Name the blood parasite species.
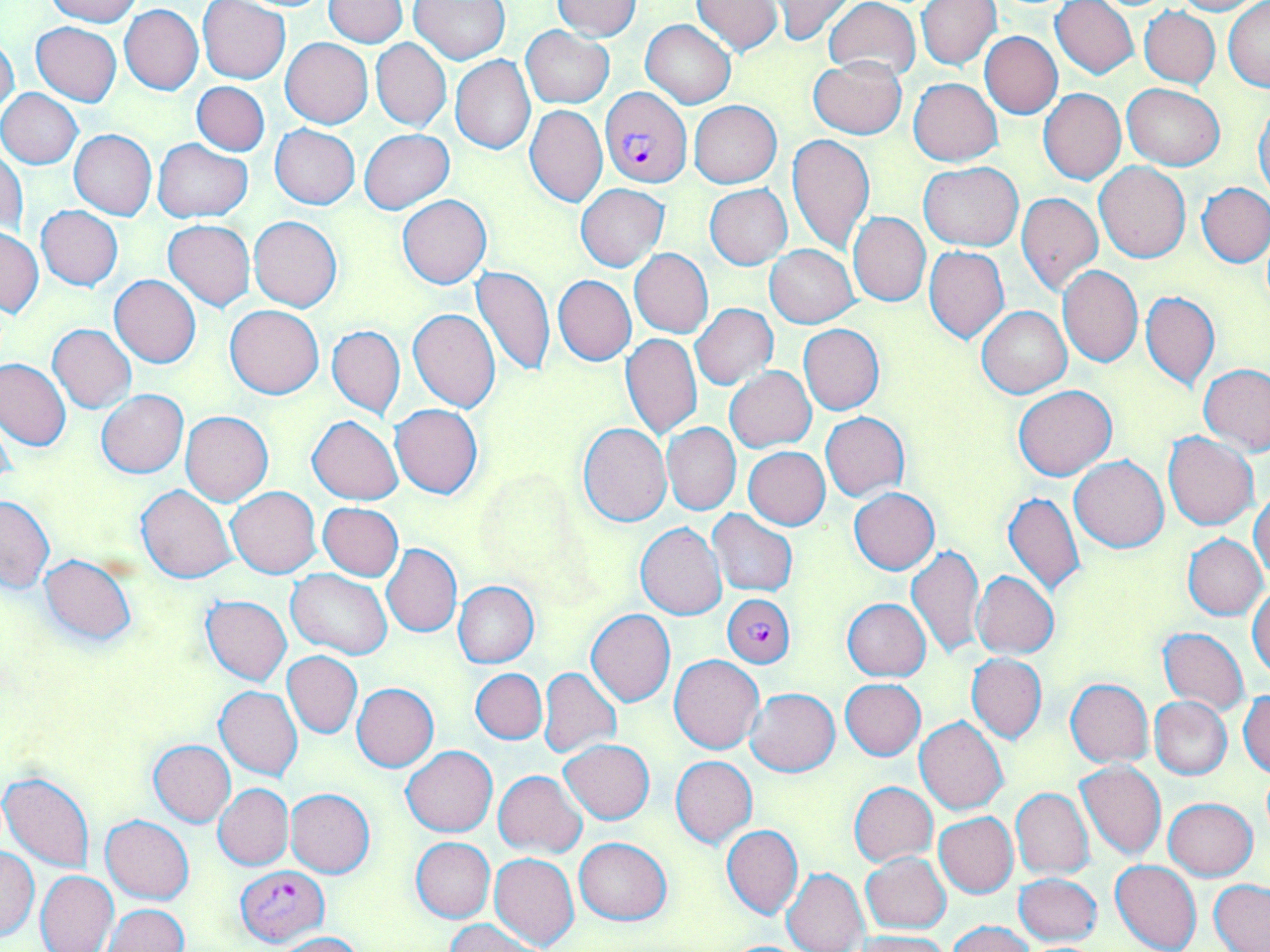

Plasmodium falciparum.

Summary:
  - Coordinate format: approximate bounding boxes as named x1/y1/x2/y2 corners in pixels
  - Uninfected red blood cell locations: (x1=44, y1=0, x2=139, y2=26), (x1=323, y1=0, x2=408, y2=47), (x1=411, y1=0, x2=510, y2=64), (x1=553, y1=0, x2=641, y2=41), (x1=771, y1=0, x2=853, y2=44), (x1=822, y1=0, x2=920, y2=81), (x1=917, y1=0, x2=1000, y2=70), (x1=1050, y1=0, x2=1139, y2=78), (x1=1167, y1=0, x2=1265, y2=15), (x1=690, y1=1, x2=784, y2=54), (x1=1223, y1=1, x2=1269, y2=90), (x1=198, y1=2, x2=290, y2=83), (x1=120, y1=5, x2=204, y2=94), (x1=1139, y1=7, x2=1220, y2=88), (x1=640, y1=20, x2=734, y2=109), (x1=30, y1=21, x2=122, y2=105), (x1=522, y1=27, x2=613, y2=108), (x1=979, y1=32, x2=1062, y2=118), (x1=0, y1=33, x2=20, y2=121), (x1=281, y1=38, x2=373, y2=128), (x1=370, y1=38, x2=450, y2=131), (x1=451, y1=55, x2=536, y2=155), (x1=809, y1=57, x2=906, y2=138), (x1=909, y1=78, x2=1002, y2=166), (x1=181, y1=82, x2=264, y2=219), (x1=192, y1=82, x2=269, y2=155), (x1=1121, y1=83, x2=1225, y2=168), (x1=0, y1=89, x2=83, y2=168), (x1=1039, y1=89, x2=1127, y2=184), (x1=689, y1=101, x2=781, y2=188), (x1=1254, y1=101, x2=1270, y2=199), (x1=525, y1=105, x2=607, y2=207), (x1=270, y1=125, x2=360, y2=209), (x1=69, y1=129, x2=156, y2=220), (x1=359, y1=129, x2=454, y2=214), (x1=787, y1=134, x2=875, y2=255), (x1=153, y1=139, x2=252, y2=222), (x1=1, y1=150, x2=27, y2=239), (x1=919, y1=162, x2=1023, y2=251), (x1=1094, y1=162, x2=1191, y2=263), (x1=576, y1=183, x2=668, y2=271), (x1=705, y1=184, x2=792, y2=268), (x1=1197, y1=184, x2=1270, y2=266), (x1=1017, y1=190, x2=1102, y2=297), (x1=398, y1=194, x2=492, y2=288), (x1=36, y1=206, x2=124, y2=290), (x1=848, y1=211, x2=930, y2=306), (x1=248, y1=215, x2=342, y2=312), (x1=163, y1=220, x2=255, y2=311), (x1=1, y1=230, x2=44, y2=317), (x1=765, y1=244, x2=858, y2=327), (x1=923, y1=246, x2=1008, y2=344), (x1=629, y1=249, x2=713, y2=337), (x1=1058, y1=265, x2=1142, y2=367), (x1=472, y1=266, x2=556, y2=378), (x1=109, y1=275, x2=201, y2=367), (x1=553, y1=275, x2=636, y2=366), (x1=1142, y1=290, x2=1219, y2=393), (x1=691, y1=304, x2=777, y2=389), (x1=225, y1=305, x2=324, y2=398), (x1=977, y1=306, x2=1071, y2=399), (x1=408, y1=308, x2=500, y2=412), (x1=48, y1=324, x2=137, y2=413), (x1=798, y1=324, x2=884, y2=414), (x1=328, y1=325, x2=405, y2=419), (x1=620, y1=333, x2=701, y2=440), (x1=0, y1=358, x2=71, y2=453), (x1=1200, y1=364, x2=1270, y2=455), (x1=725, y1=367, x2=815, y2=452), (x1=1013, y1=385, x2=1117, y2=481), (x1=96, y1=390, x2=188, y2=477), (x1=390, y1=404, x2=483, y2=499), (x1=181, y1=411, x2=272, y2=504), (x1=821, y1=412, x2=909, y2=501), (x1=307, y1=415, x2=403, y2=505), (x1=578, y1=422, x2=672, y2=526), (x1=662, y1=423, x2=741, y2=515), (x1=1164, y1=432, x2=1258, y2=530), (x1=744, y1=447, x2=830, y2=530), (x1=1070, y1=456, x2=1169, y2=552), (x1=136, y1=486, x2=236, y2=583), (x1=227, y1=487, x2=321, y2=578), (x1=850, y1=489, x2=939, y2=574), (x1=1250, y1=490, x2=1270, y2=580), (x1=1003, y1=492, x2=1085, y2=596), (x1=0, y1=497, x2=55, y2=593), (x1=318, y1=502, x2=403, y2=580), (x1=707, y1=511, x2=796, y2=596), (x1=635, y1=521, x2=726, y2=619), (x1=1183, y1=533, x2=1267, y2=618), (x1=383, y1=544, x2=461, y2=636), (x1=907, y1=545, x2=983, y2=659), (x1=38, y1=555, x2=136, y2=645), (x1=287, y1=569, x2=393, y2=659), (x1=972, y1=571, x2=1059, y2=659), (x1=454, y1=582, x2=539, y2=667), (x1=1249, y1=585, x2=1269, y2=679), (x1=202, y1=595, x2=291, y2=685), (x1=843, y1=598, x2=930, y2=681), (x1=586, y1=610, x2=675, y2=706), (x1=1158, y1=627, x2=1249, y2=715), (x1=283, y1=651, x2=362, y2=737), (x1=670, y1=654, x2=764, y2=753), (x1=966, y1=654, x2=1046, y2=743), (x1=471, y1=668, x2=547, y2=743), (x1=539, y1=668, x2=621, y2=758), (x1=840, y1=678, x2=925, y2=760), (x1=1064, y1=679, x2=1153, y2=767), (x1=352, y1=684, x2=439, y2=771), (x1=215, y1=687, x2=302, y2=781), (x1=745, y1=688, x2=839, y2=776), (x1=1239, y1=690, x2=1269, y2=778), (x1=1149, y1=696, x2=1233, y2=780), (x1=915, y1=717, x2=1008, y2=814), (x1=561, y1=739, x2=654, y2=824), (x1=148, y1=740, x2=236, y2=826), (x1=402, y1=746, x2=497, y2=836), (x1=671, y1=756, x2=757, y2=848), (x1=1075, y1=762, x2=1166, y2=862), (x1=494, y1=770, x2=587, y2=857), (x1=1, y1=772, x2=95, y2=873), (x1=213, y1=783, x2=293, y2=871), (x1=850, y1=783, x2=937, y2=866), (x1=1010, y1=787, x2=1094, y2=879), (x1=286, y1=789, x2=375, y2=877), (x1=1164, y1=797, x2=1257, y2=879), (x1=934, y1=813, x2=1018, y2=897), (x1=101, y1=815, x2=193, y2=904), (x1=722, y1=825, x2=802, y2=918), (x1=412, y1=837, x2=494, y2=922), (x1=574, y1=838, x2=672, y2=925), (x1=0, y1=845, x2=38, y2=942), (x1=490, y1=852, x2=581, y2=950), (x1=861, y1=853, x2=951, y2=934), (x1=1110, y1=860, x2=1202, y2=952), (x1=782, y1=868, x2=869, y2=952), (x1=35, y1=869, x2=119, y2=952), (x1=1014, y1=874, x2=1102, y2=945), (x1=1208, y1=880, x2=1270, y2=951), (x1=104, y1=904, x2=189, y2=952), (x1=447, y1=918, x2=538, y2=952), (x1=946, y1=920, x2=1038, y2=952), (x1=852, y1=931, x2=950, y2=952), (x1=277, y1=932, x2=365, y2=952)
  - Plasmodium falciparum-infected red blood cell locations: (x1=601, y1=87, x2=692, y2=187), (x1=720, y1=593, x2=793, y2=664), (x1=235, y1=866, x2=327, y2=946)
  - Modality: optical microscopy
  - Field of view: single
  - Preparation: thin blood film
  - Image size: 1270×952 pixels
  - Magnification: 1000x
  - Stain: May-Grünwald-Giemsa